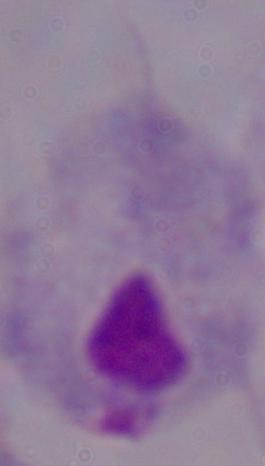
modality = photomicrograph
identification = trichomonad
magnification = 1000x